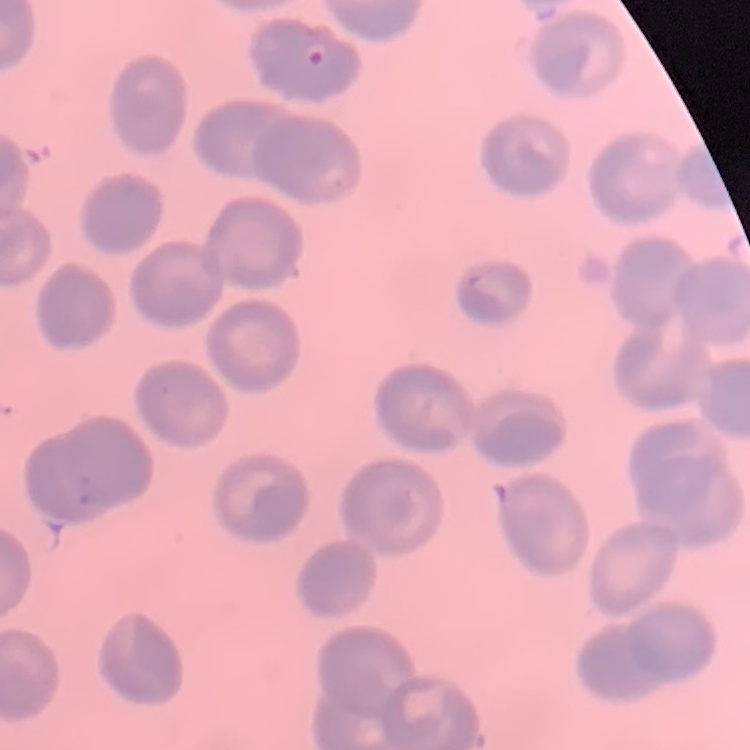

erythrocyte morphology = no rouleaux formation
preparation = thin peripheral smear
stain = Field's or Giemsa
image type = square crop of a larger photomicrograph